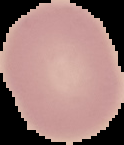 From a thin blood film. Result: negative for malaria parasites. Image is 124×145 pixels. Segmented cell region on a black background.